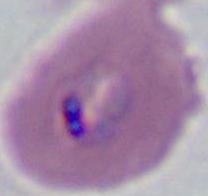
identification = Plasmodium
modality = photomicrograph
magnification = 400x or 1000x